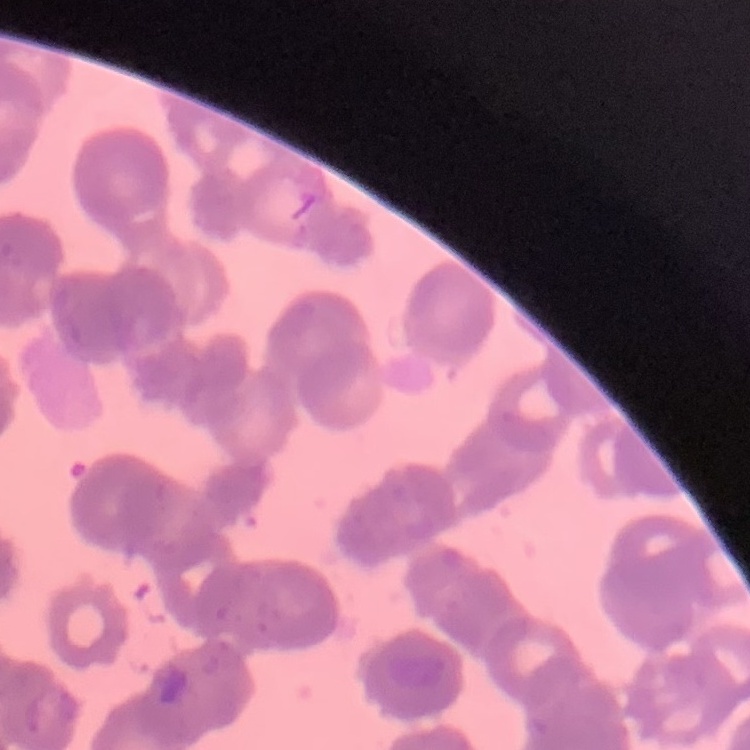

{
  "red_blood_cell_morphology": "rouleaux formation",
  "preparation": "thin blood film",
  "stain": "Field's or Giemsa",
  "image_type": "one tile cut from a larger photomicrograph"
}